Give the location of every parasitized RBC.
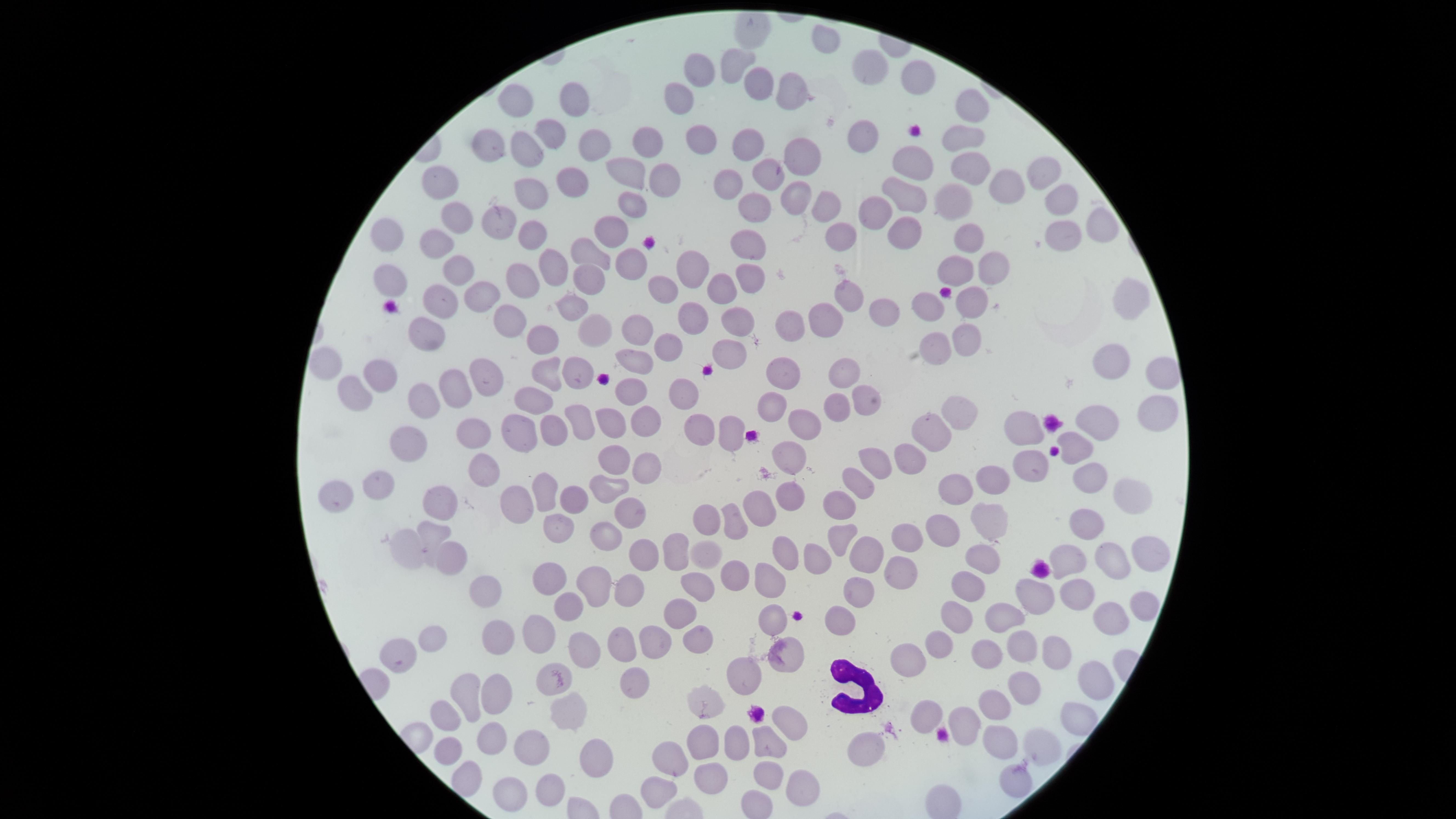

No parasitized RBCs identified.

Approximate marker points as (x, y) in pixels. WBCs: (857, 692). Uninfected RBCs: (821, 44), (734, 63), (871, 69), (699, 70), (920, 74), (767, 84), (791, 92), (683, 100), (972, 100), (576, 103), (517, 107), (864, 132), (555, 133), (963, 140), (697, 141), (591, 143), (649, 144), (750, 145), (488, 147), (525, 147), (805, 151), (915, 167), (968, 169), (633, 170), (1045, 171), (775, 174), (665, 178), (566, 182), (442, 184), (1006, 185), (729, 191), (528, 195), (909, 196), (1060, 196), (797, 197), (961, 203), (827, 204), (633, 208), (762, 208), (462, 214), (876, 217), (496, 219), (1104, 219), (910, 229), (616, 232), (843, 233), (392, 236), (971, 237), (529, 239), (1056, 240), (439, 244), (756, 250), (595, 255), (629, 259), (455, 265), (555, 266), (687, 267), (954, 267), (993, 267), (753, 277), (592, 280), (392, 281), (529, 281), (728, 289), (484, 292), (668, 292), (847, 296), (435, 302), (974, 303), (931, 304), (572, 306), (1130, 306), (889, 310), (738, 315), (692, 317), (506, 318), (823, 318), (786, 322), (424, 329), (636, 329), (595, 330), (539, 332), (965, 337), (669, 343), (931, 347), (736, 354), (633, 357), (326, 359), (1115, 366), (550, 372), (383, 373), (847, 373), (579, 376), (1161, 376), (490, 377), (786, 377), (459, 384), (358, 391), (636, 391), (858, 396), (533, 398), (681, 398), (424, 399), (772, 406), (842, 406), (644, 414), (1155, 415), (584, 418), (964, 418), (610, 421), (1104, 421), (801, 424), (555, 429), (524, 431), (705, 431), (1033, 431), (483, 433), (731, 433), (942, 433), (418, 442), (1082, 447), (917, 448), (791, 451), (613, 459), (646, 462), (874, 462), (1033, 463), (1092, 473), (482, 474), (990, 476), (858, 483), (376, 485), (603, 486), (955, 489), (546, 491), (1125, 496), (339, 497), (785, 497), (438, 500), (516, 500), (839, 501), (573, 502), (760, 504), (627, 508), (985, 517), (1085, 518), (729, 519), (554, 520), (703, 520), (428, 529), (602, 532), (838, 533), (903, 535), (939, 535), (407, 544), (668, 547), (1141, 552), (783, 553), (858, 553), (639, 554), (702, 556), (1074, 556), (814, 557), (447, 559), (982, 559), (1113, 562), (901, 573), (727, 575), (550, 577), (767, 577), (964, 579), (594, 581), (626, 588), (698, 588), (857, 590), (484, 591), (1035, 594), (1078, 594), (565, 603), (1136, 606), (682, 612), (776, 615), (1106, 615), (960, 617), (842, 621), (1009, 623), (541, 632), (438, 638), (499, 638), (650, 639), (695, 639), (615, 640), (935, 644), (581, 646), (402, 648), (1020, 650), (1055, 652), (787, 655), (986, 655), (908, 663), (1092, 672), (751, 674), (546, 678), (627, 681), (1019, 688), (493, 693), (462, 694), (706, 699), (572, 707), (993, 707), (448, 712), (930, 716), (784, 721), (963, 721), (704, 737), (487, 738), (995, 739), (770, 742), (1035, 742), (865, 743), (448, 747), (728, 747), (527, 749), (596, 757), (668, 765), (463, 772), (1016, 778), (711, 779), (769, 780), (547, 784), (793, 784), (515, 790), (658, 791). Giemsa stain. The visible region is circular. Photographed with a smartphone camera through the microscope eyepiece. Thin blood smear. Image is 1456×819 pixels. One field of view of the specimen.